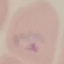

malaria_status: parasitized
preparation: thin blood smear
capture: smartphone camera at the microscope eyepiece
stain: Giemsa
image_type: cell patch, automatically extracted from a larger field of view and resized to 64 × 64 pixels